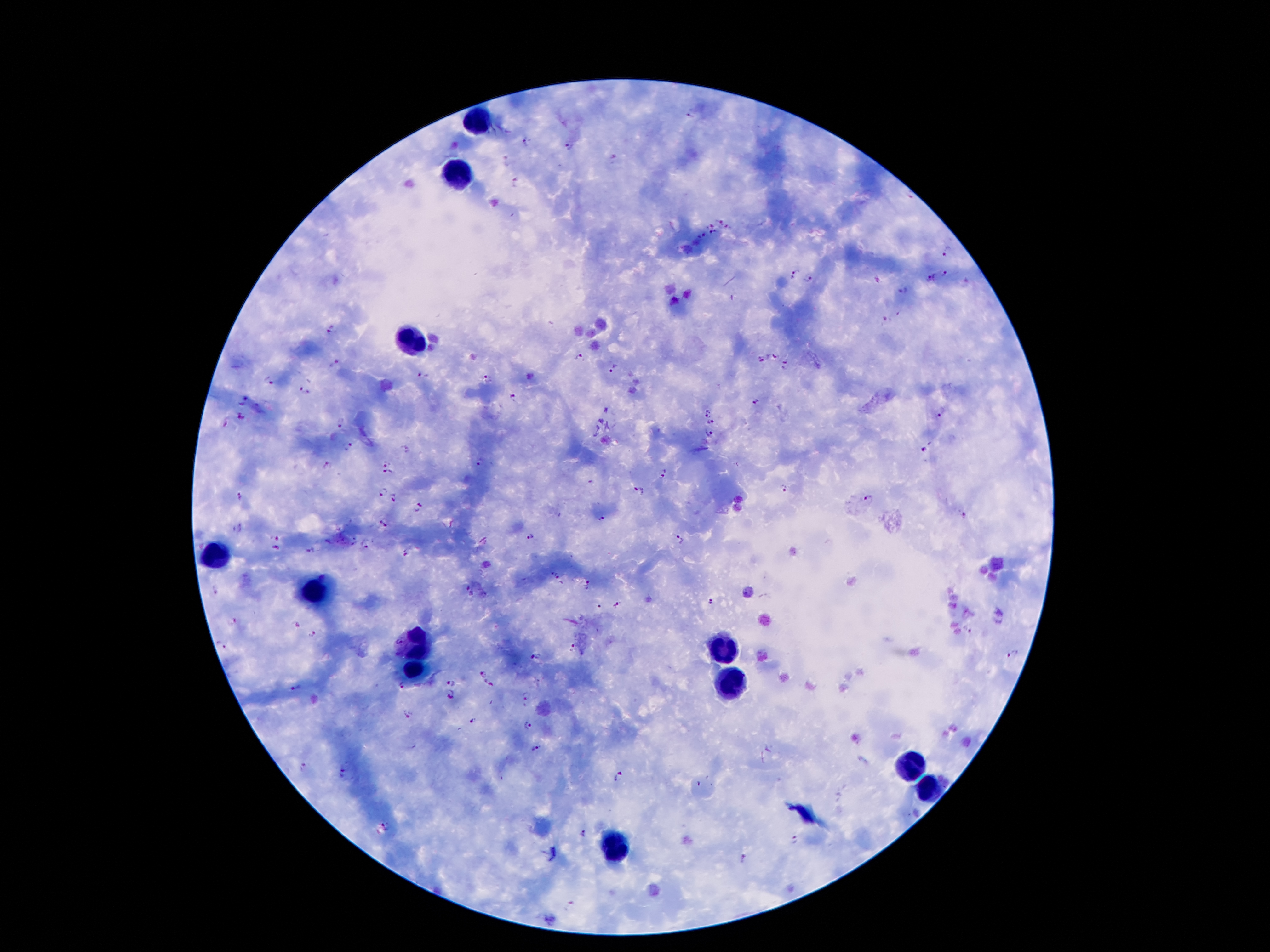 Approximate object centers, in pixels from the top-left corner. Leukocyte locations: (x=477, y=121), (x=460, y=178), (x=410, y=338), (x=215, y=553), (x=319, y=590), (x=722, y=645), (x=415, y=647), (x=413, y=672), (x=734, y=679), (x=910, y=763), (x=927, y=788), (x=620, y=847). Plasmodium parasite locations: (x=691, y=116), (x=527, y=140), (x=568, y=146), (x=613, y=158), (x=507, y=161), (x=516, y=184), (x=721, y=220), (x=711, y=225), (x=729, y=228), (x=702, y=234), (x=714, y=234), (x=949, y=250), (x=946, y=273), (x=794, y=275), (x=932, y=277), (x=808, y=279), (x=902, y=291), (x=885, y=321), (x=331, y=333), (x=773, y=354), (x=579, y=357), (x=761, y=360), (x=335, y=365), (x=785, y=365), (x=612, y=368), (x=422, y=375), (x=487, y=378), (x=270, y=383), (x=303, y=391), (x=512, y=399), (x=243, y=401), (x=756, y=401), (x=941, y=410), (x=705, y=412), (x=240, y=417), (x=341, y=422), (x=710, y=422), (x=225, y=424), (x=708, y=434), (x=348, y=446), (x=406, y=448), (x=926, y=448), (x=387, y=461), (x=479, y=463), (x=327, y=466), (x=387, y=472), (x=662, y=474), (x=784, y=489), (x=640, y=491), (x=383, y=493), (x=240, y=496), (x=396, y=499), (x=869, y=499), (x=420, y=507), (x=962, y=513), (x=601, y=520), (x=384, y=522), (x=237, y=529), (x=277, y=537), (x=530, y=538), (x=679, y=538), (x=353, y=541), (x=365, y=544), (x=277, y=548), (x=311, y=551), (x=405, y=553), (x=558, y=576), (x=588, y=585), (x=466, y=587), (x=217, y=590), (x=709, y=604), (x=600, y=605), (x=621, y=605), (x=232, y=621), (x=968, y=630), (x=314, y=634), (x=396, y=641), (x=219, y=645), (x=572, y=648), (x=1012, y=655), (x=534, y=658), (x=484, y=671), (x=450, y=682), (x=403, y=684), (x=490, y=684), (x=296, y=688), (x=451, y=695), (x=525, y=695), (x=408, y=714), (x=474, y=721), (x=529, y=726), (x=535, y=749), (x=303, y=766), (x=342, y=771), (x=620, y=776), (x=386, y=826), (x=584, y=835), (x=795, y=839), (x=744, y=859), (x=571, y=904). 100x magnification. Patient malaria status: positive for Plasmodium falciparum. Thick blood film. One field from this slide. Giemsa-stained preparation. Photographed through the microscope eyepiece with a smartphone camera. Image is 1270×952 pixels.